Locate every blood parasite and identify its species.
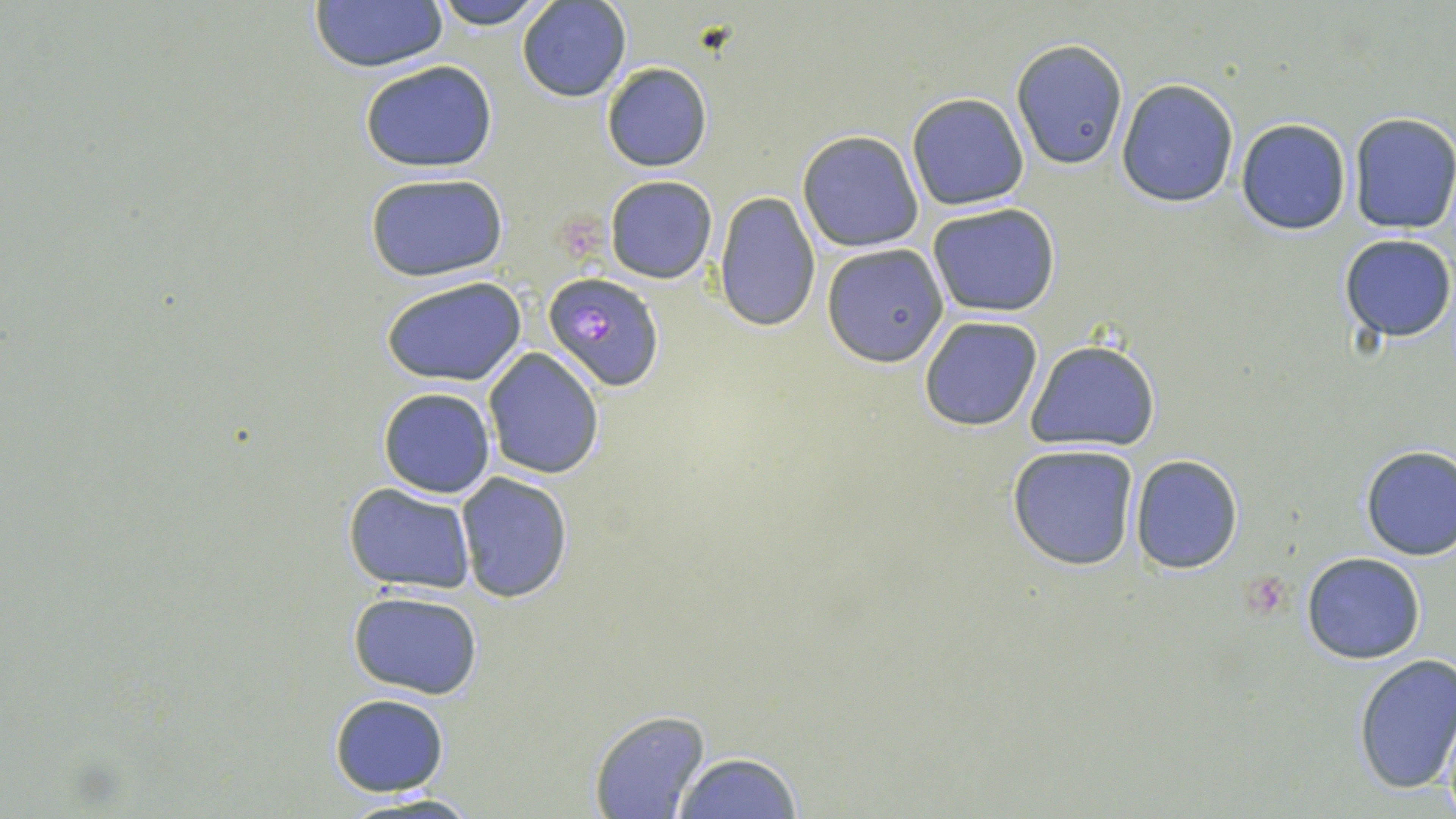
Approximate bounding boxes as (x1,y1)-(x2,y2) corner pairs in pixels.
Plasmodium falciparum-infected red blood cells: (542,272)-(666,393).
No Plasmodium ovale, Plasmodium malariae, Plasmodium vivax, Babesia divergens, or Trypanosoma brucei observed.

slide-level diagnosis = Plasmodium falciparum
modality = optical microscopy
preparation = thin blood film
magnification = 1000x
image size = 1456×819 pixels
field of view = single
uninfected red blood cell locations = approximate bounding boxes as (x1,y1)-(x2,y2) corner pairs in pixels: (428,0)-(553,28), (517,0)-(632,102), (309,2)-(448,72), (1011,37)-(1128,169), (358,60)-(499,171), (601,62)-(712,172), (1115,79)-(1240,207), (906,93)-(1030,211), (1349,112)-(1456,234), (1237,118)-(1351,235), (797,129)-(924,252), (364,170)-(509,282), (605,175)-(718,284), (712,191)-(820,332), (928,203)-(1060,316), (1340,233)-(1456,343), (820,246)-(947,365), (383,277)-(527,386), (919,315)-(1045,431), (1025,339)-(1159,451), (481,348)-(604,479), (377,388)-(495,498), (1007,443)-(1139,571), (1358,445)-(1455,561), (1129,455)-(1245,573), (455,472)-(574,605), (343,482)-(476,592), (1302,552)-(1426,664), (348,589)-(484,700), (1351,654)-(1456,797), (328,693)-(450,797), (587,709)-(710,819), (1435,719)-(1456,818), (670,751)-(805,819), (336,790)-(487,818)
stain = May-Grünwald-Giemsa